Give the position of every Plasmodium parasite and every leukocyte.
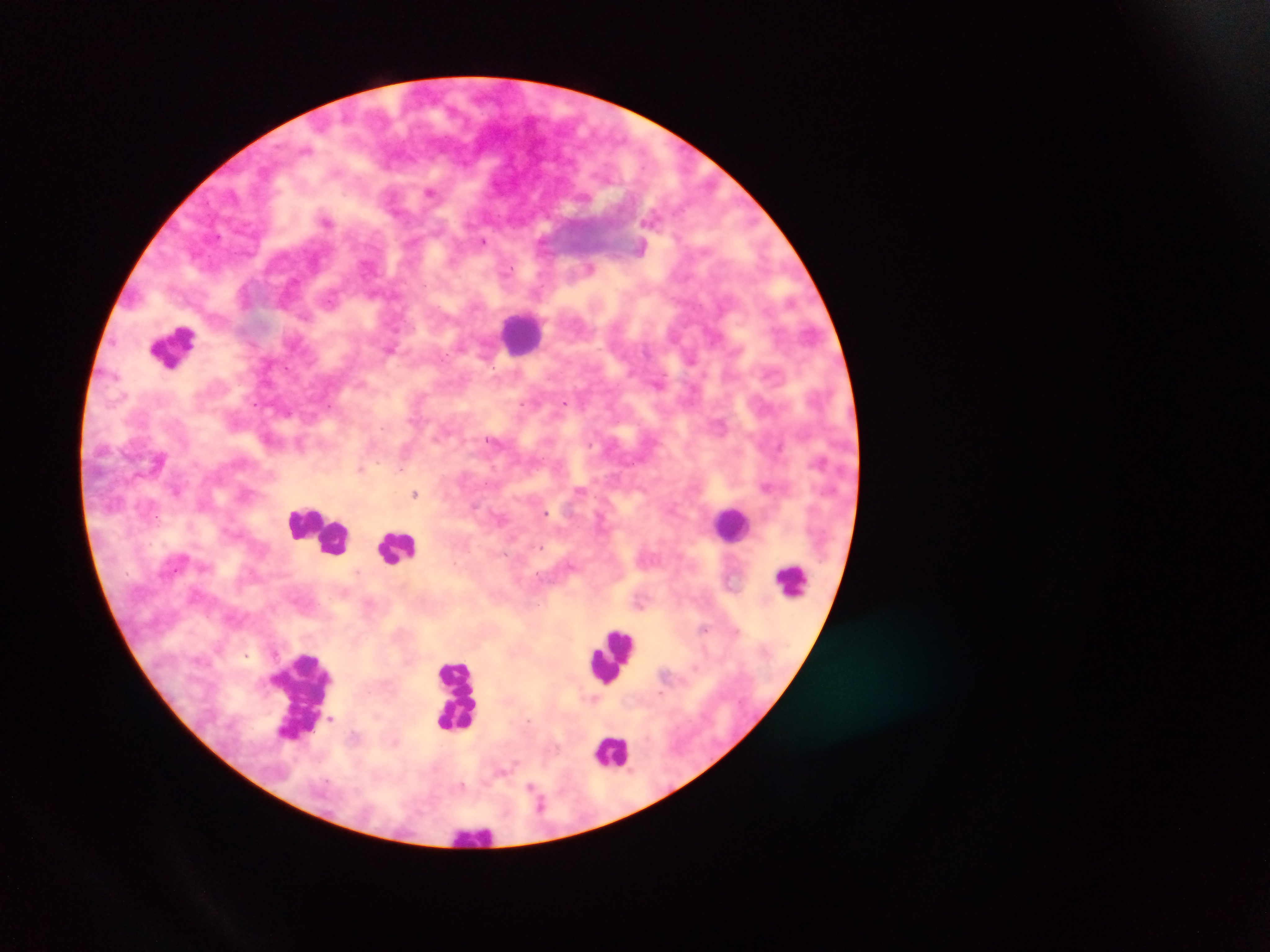

Approximate centers as {x, y} in pixels.
Plasmodium parasites: {432, 192}, {326, 220}, {483, 241}, {641, 246}, {590, 266}, {391, 349}, {565, 402}, {289, 411}, {493, 440}, {301, 444}, {361, 468}, {766, 486}, {177, 490}, {415, 493}, {545, 512}, {331, 718}.
Leukocytes: {522, 332}, {173, 347}, {732, 524}, {323, 529}, {398, 547}, {792, 580}, {614, 654}, {300, 695}, {458, 697}, {611, 751}, {476, 834}.

{
  "image_size": "1270×952 pixels",
  "capture": "mobile-phone photograph through a microscope",
  "preparation": "thick blood smear",
  "field_of_view": "single",
  "country": "Ghana"
}